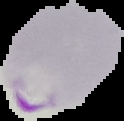

image size = 124×121 pixels
preparation = thin blood film
image type = segmented cell region on a black background
result = malaria parasites detected